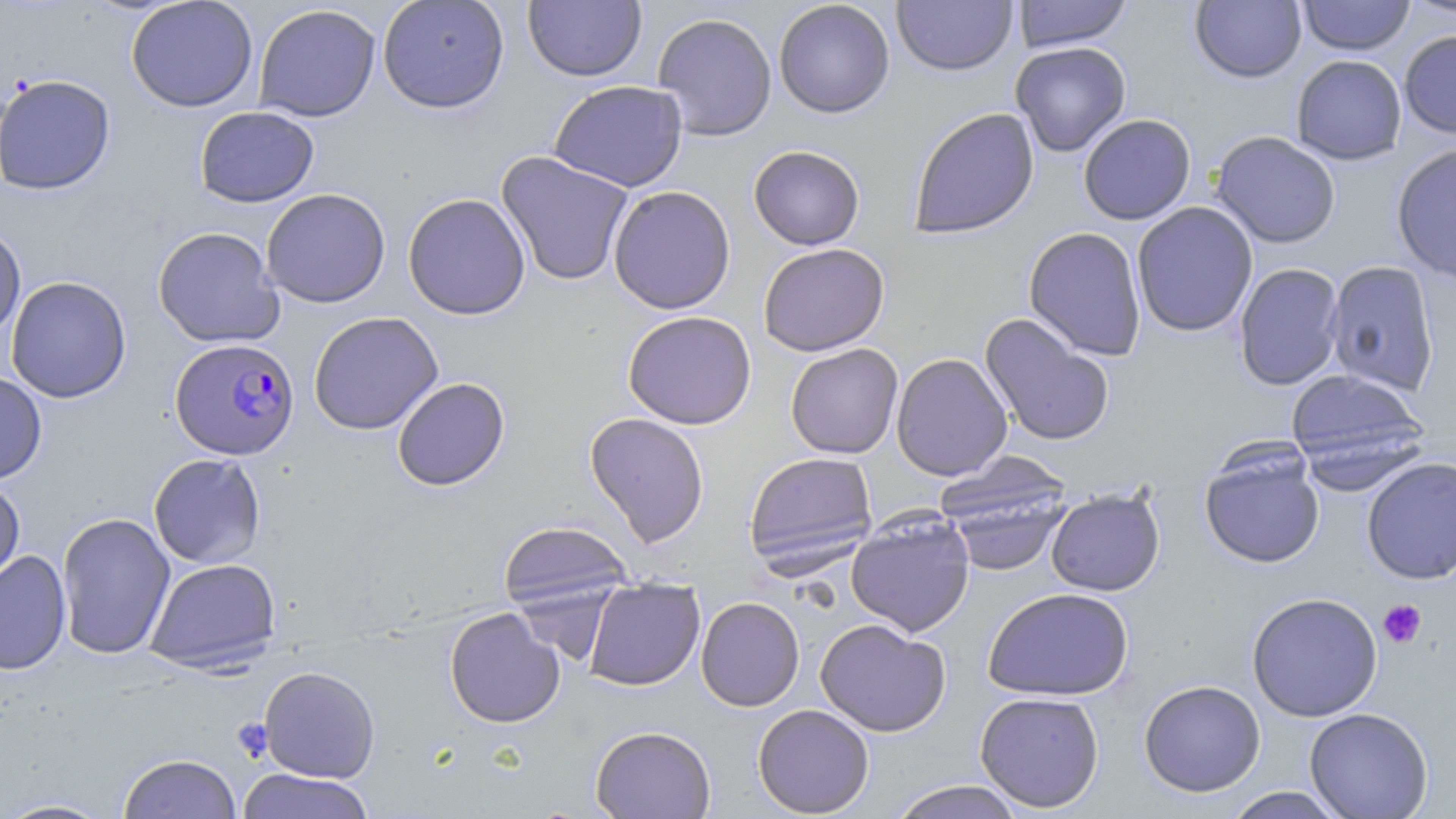

Summary:
  - Coordinate format: approximate bounding boxes as named x1/y1/x2/y2 corners in pixels
  - Plasmodium falciparum-infected red blood cell locations: (x1=170, y1=338, x2=300, y2=461)
  - Platelet locations: (x1=1377, y1=599, x2=1427, y2=649)
  - Uninfected red blood cell locations: (x1=126, y1=0, x2=258, y2=113), (x1=377, y1=0, x2=510, y2=113), (x1=773, y1=0, x2=895, y2=118), (x1=1013, y1=0, x2=1132, y2=51), (x1=1297, y1=0, x2=1415, y2=56), (x1=1402, y1=0, x2=1456, y2=20), (x1=524, y1=1, x2=646, y2=82), (x1=891, y1=1, x2=1017, y2=76), (x1=1190, y1=1, x2=1307, y2=83), (x1=253, y1=4, x2=381, y2=122), (x1=652, y1=12, x2=778, y2=141), (x1=1399, y1=29, x2=1456, y2=139), (x1=1011, y1=42, x2=1131, y2=157), (x1=1291, y1=54, x2=1407, y2=165), (x1=0, y1=73, x2=116, y2=195), (x1=548, y1=80, x2=688, y2=192), (x1=194, y1=106, x2=319, y2=208), (x1=908, y1=107, x2=1039, y2=240), (x1=1078, y1=113, x2=1196, y2=225), (x1=1211, y1=131, x2=1341, y2=248), (x1=1391, y1=142, x2=1456, y2=283), (x1=749, y1=145, x2=865, y2=250), (x1=495, y1=150, x2=635, y2=286), (x1=608, y1=185, x2=736, y2=314), (x1=260, y1=188, x2=391, y2=308), (x1=402, y1=192, x2=531, y2=320), (x1=1132, y1=202, x2=1258, y2=337), (x1=0, y1=223, x2=26, y2=343), (x1=152, y1=226, x2=284, y2=348), (x1=1023, y1=227, x2=1147, y2=360), (x1=758, y1=242, x2=889, y2=357), (x1=1324, y1=260, x2=1440, y2=396), (x1=1234, y1=262, x2=1345, y2=390), (x1=6, y1=276, x2=131, y2=403), (x1=622, y1=310, x2=756, y2=430), (x1=308, y1=311, x2=444, y2=435), (x1=979, y1=313, x2=1115, y2=447), (x1=785, y1=343, x2=903, y2=459), (x1=891, y1=353, x2=1013, y2=481), (x1=1285, y1=367, x2=1429, y2=477), (x1=0, y1=371, x2=48, y2=484), (x1=392, y1=377, x2=510, y2=491), (x1=585, y1=412, x2=710, y2=547), (x1=1199, y1=447, x2=1326, y2=569), (x1=744, y1=451, x2=878, y2=572), (x1=148, y1=453, x2=267, y2=569), (x1=935, y1=456, x2=1074, y2=574), (x1=1362, y1=456, x2=1456, y2=584), (x1=0, y1=478, x2=25, y2=594), (x1=1045, y1=487, x2=1166, y2=597), (x1=56, y1=511, x2=176, y2=660), (x1=846, y1=511, x2=975, y2=638), (x1=498, y1=519, x2=634, y2=612), (x1=0, y1=550, x2=71, y2=675), (x1=144, y1=557, x2=282, y2=673), (x1=583, y1=578, x2=705, y2=691), (x1=983, y1=587, x2=1135, y2=701), (x1=1246, y1=591, x2=1383, y2=722), (x1=696, y1=596, x2=805, y2=711), (x1=444, y1=607, x2=565, y2=728), (x1=815, y1=618, x2=951, y2=737), (x1=259, y1=665, x2=380, y2=782), (x1=1138, y1=679, x2=1266, y2=796), (x1=974, y1=691, x2=1105, y2=812), (x1=752, y1=704, x2=875, y2=817), (x1=1304, y1=707, x2=1434, y2=818), (x1=590, y1=725, x2=716, y2=818), (x1=117, y1=753, x2=241, y2=819), (x1=236, y1=768, x2=376, y2=819), (x1=888, y1=780, x2=1026, y2=819), (x1=1221, y1=787, x2=1349, y2=818), (x1=1, y1=797, x2=115, y2=818)
  - Slide-level diagnosis: Plasmodium falciparum
  - Magnification: 1000x
  - Stain: May-Grünwald-Giemsa
  - Field of view: one of a larger specimen
  - Preparation: thin blood film
  - Modality: light microscopy
  - Image size: 1456×819 pixels